Give the preparation type.
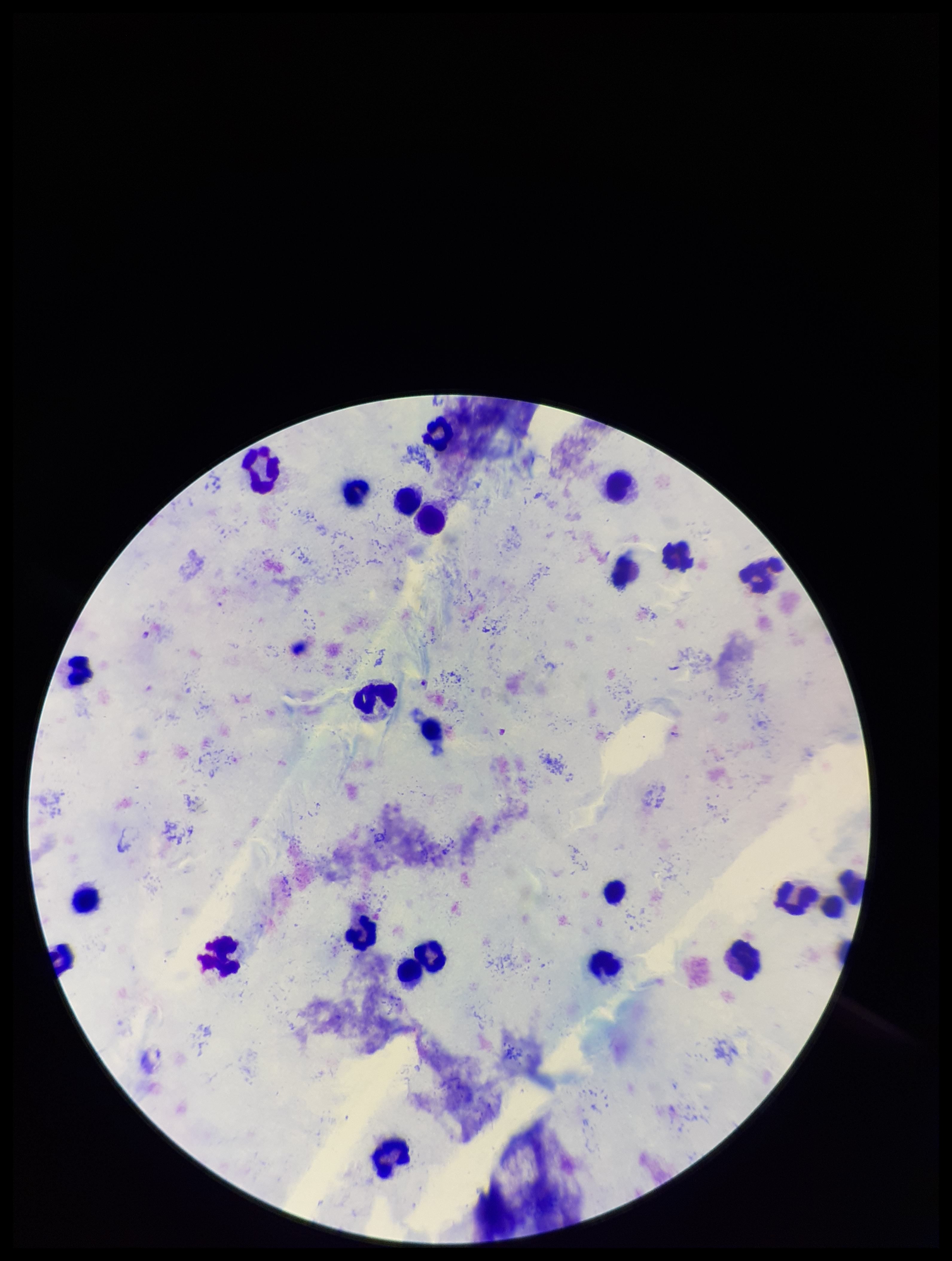
It is a thick blood smear.

Stained with Giemsa. Patient malaria status: infected. Smartphone photograph taken through the eyepiece of a microscope. Image is 952×1261 pixels. Leukocyte count: 24. Parasite count: 0. Species reported for this patient: Plasmodium falciparum. Plasmodium parasites: none detected. One field from this slide.